Assess the morphology of the erythrocytes.
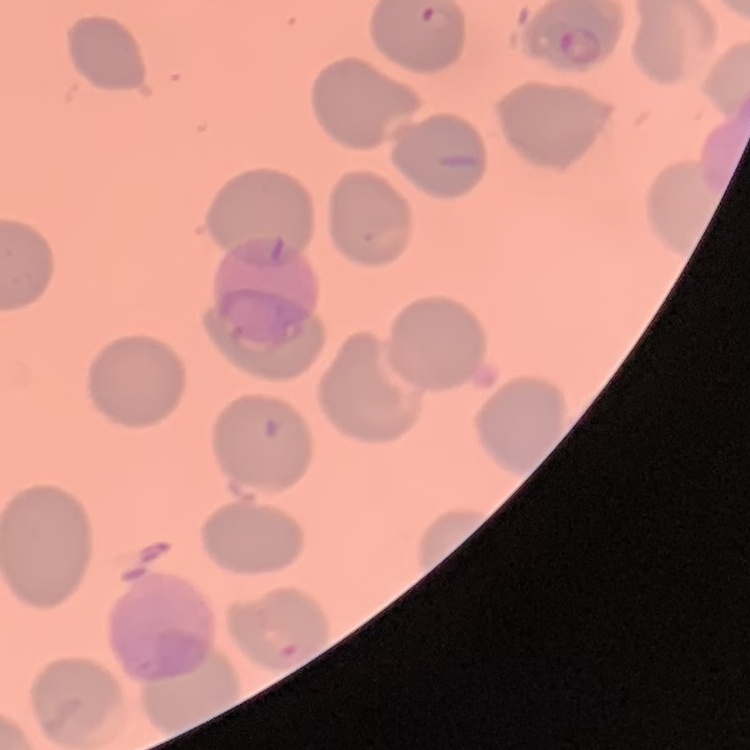

They show no rouleaux formation.

Square crop of a larger photomicrograph. Thin peripheral smear. Field's or Giemsa stain.